Point out every Plasmodium parasite.
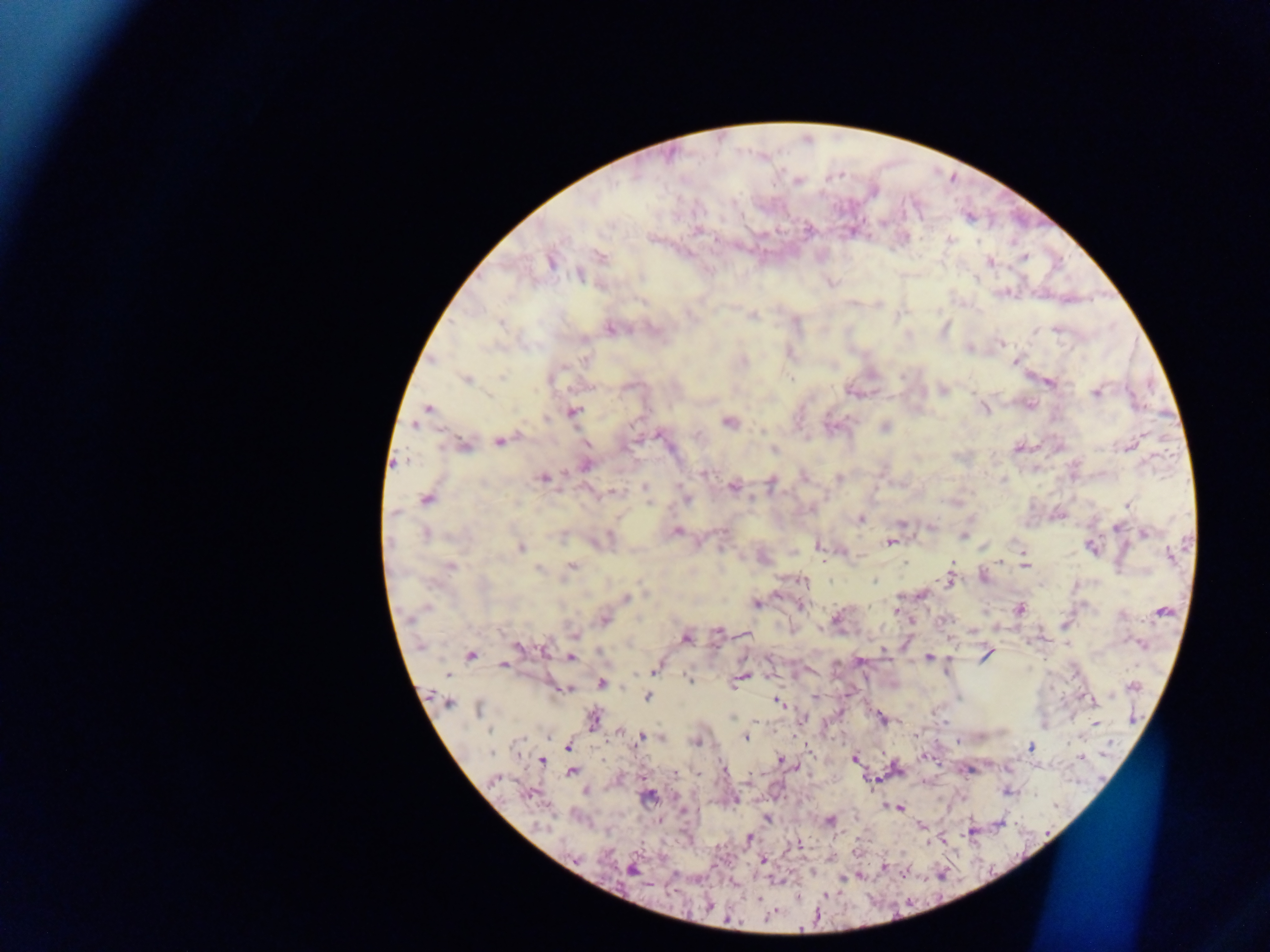

Approximate centers as [x, y] in pixels.
Plasmodium parasites: [698, 230], [950, 239], [600, 256], [1024, 257], [551, 261], [989, 261], [580, 275], [751, 316], [500, 324], [611, 328], [1056, 330], [1035, 332], [1001, 343], [790, 354], [586, 359], [1014, 361], [502, 377], [467, 380], [791, 380], [1049, 383], [942, 390], [1096, 393], [428, 408], [984, 409], [573, 412], [545, 418], [730, 421], [415, 425], [885, 427], [499, 442], [463, 445], [1129, 447], [1017, 448], [774, 451], [585, 465], [705, 474], [543, 477], [804, 477], [839, 478], [1004, 479], [771, 483], [645, 487], [733, 487], [614, 492], [427, 499], [686, 499], [649, 503], [1127, 505], [812, 509], [394, 513], [860, 519], [901, 523], [931, 527], [1116, 528], [677, 531], [1145, 533], [425, 535], [963, 537], [890, 542], [819, 547], [521, 548], [1092, 548], [1170, 556], [1000, 561], [905, 563], [572, 565], [450, 566], [1026, 566], [569, 568], [538, 569], [984, 577], [948, 578], [804, 581], [874, 581], [921, 595], [626, 597], [757, 604], [800, 606], [426, 608], [1018, 610], [896, 611], [1163, 612], [836, 618], [604, 619], [944, 620], [717, 631], [574, 636], [686, 638], [1141, 643], [518, 649], [544, 649], [884, 651], [601, 653], [471, 655], [985, 655], [928, 657], [570, 658], [860, 662], [504, 665], [654, 671], [447, 674], [742, 677], [689, 679], [601, 684], [1133, 687], [562, 689], [647, 697], [814, 697], [1091, 699], [779, 702], [447, 703], [479, 709], [593, 719], [802, 719], [882, 719], [1096, 723], [490, 730], [745, 737], [640, 738], [661, 738], [696, 742], [568, 745], [1031, 747], [492, 753], [1083, 757], [855, 759], [781, 760], [542, 761], [572, 771], [495, 779], [528, 794], [649, 796], [735, 799], [899, 808], [767, 819], [830, 822], [749, 838], [798, 845], [763, 860], [632, 870], [758, 898].

Single field of view. Sample from Ghana. Thick blood film. Image is 1270×952 pixels. Photographed through a microscope with a mobile-phone camera.